Give the extent of all Plasmodium falciparum-infected red blood cells.
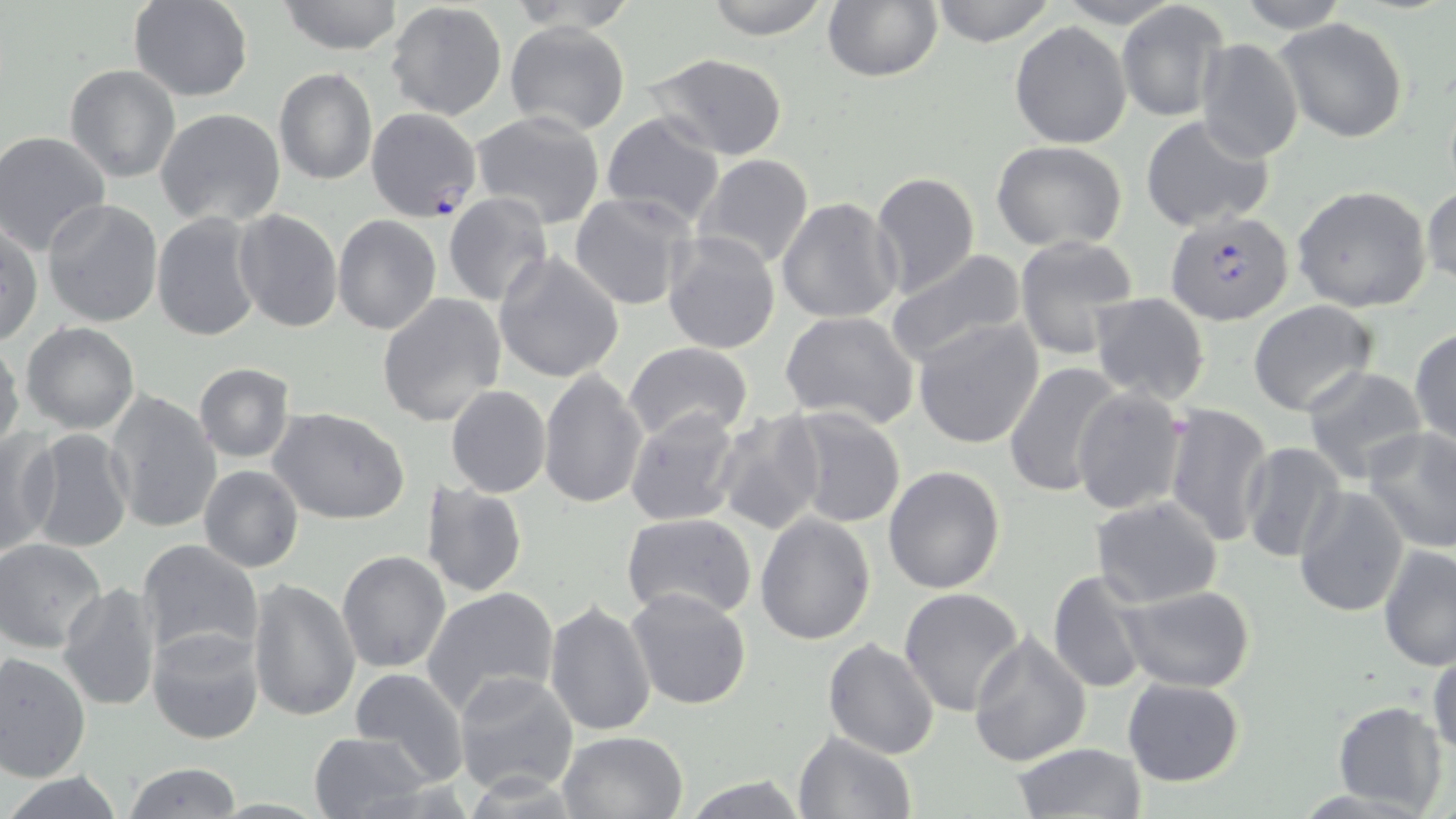
Approximate bounding boxes as (x1,y1)-(x2,y2) corner pairs in pixels.
Plasmodium falciparum-infected red blood cells: (1166,210)-(1294,325).

Uninfected red blood cell locations: (129,0)-(253,101), (276,0)-(406,55), (703,0)-(830,39), (928,0)-(1059,47), (1231,0)-(1352,32), (385,1)-(508,119), (504,1)-(641,31), (822,1)-(942,82), (1117,2)-(1228,123), (1275,18)-(1409,144), (503,20)-(631,136), (1010,21)-(1132,148), (1195,37)-(1303,163), (645,53)-(789,161), (65,64)-(181,183), (273,66)-(377,185), (365,106)-(482,224), (155,108)-(286,229), (470,110)-(605,229), (599,110)-(726,228), (1141,117)-(1275,230), (1,131)-(110,254), (992,141)-(1130,252), (694,154)-(816,273), (868,171)-(980,300), (1421,183)-(1456,289), (1292,185)-(1434,312), (569,192)-(696,312), (442,193)-(554,308), (775,196)-(902,324), (42,199)-(164,328), (232,209)-(343,332), (152,213)-(264,342), (333,215)-(441,334), (2,222)-(43,346), (662,231)-(780,354), (1014,234)-(1139,360), (885,250)-(1030,369), (494,251)-(625,383), (1090,292)-(1210,406), (377,294)-(508,428), (1248,299)-(1379,416), (778,308)-(921,430), (912,317)-(1046,450), (22,322)-(140,434), (1410,326)-(1456,450), (0,334)-(25,454), (624,342)-(753,443), (1005,362)-(1128,500), (194,364)-(295,463), (1303,366)-(1429,483), (538,368)-(647,509), (446,385)-(551,498), (1072,386)-(1189,516), (105,388)-(222,535), (1163,401)-(1275,548), (624,406)-(744,529), (782,406)-(906,528), (269,408)-(412,527), (713,409)-(828,538), (23,428)-(134,553), (1364,428)-(1456,553), (0,430)-(59,559), (1239,441)-(1345,562), (198,465)-(304,573), (882,465)-(1005,594), (421,481)-(527,598), (1293,484)-(1411,618), (1090,495)-(1223,606), (620,513)-(758,624), (754,513)-(875,646), (0,539)-(110,653), (135,539)-(264,665), (1378,544)-(1456,671), (336,551)-(452,674), (1046,568)-(1155,695), (246,579)-(360,723), (57,582)-(164,711), (1119,585)-(1257,691), (423,586)-(560,715), (625,587)-(752,711), (899,588)-(1025,718), (543,601)-(657,738), (147,625)-(267,745), (968,631)-(1092,766), (823,636)-(941,758), (1430,644)-(1456,763), (0,651)-(92,781), (349,667)-(469,786), (454,670)-(580,796), (1122,678)-(1247,786), (1333,702)-(1449,814), (557,729)-(689,819), (306,731)-(435,818), (794,731)-(915,818), (1014,742)-(1146,819), (123,763)-(244,818), (2,770)-(126,819), (678,774)-(814,817). Slide-level diagnosis: Plasmodium falciparum. Captured at 1000x magnification. Thin blood smear. Light microscopy. Image is 1456×819 pixels. May-Grünwald-Giemsa-stained preparation. One field of a larger specimen.